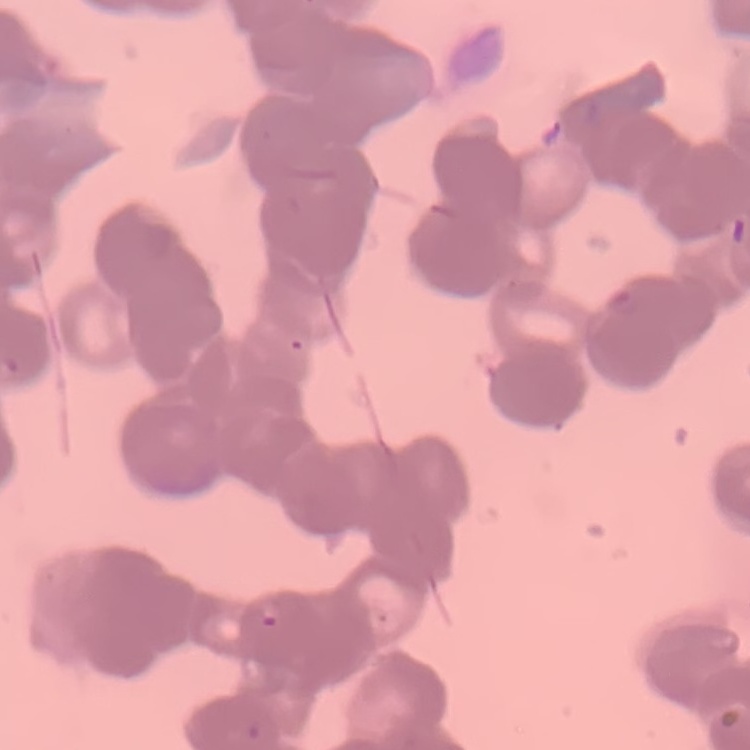
The erythrocytes exhibit rouleaux formation. Square crop of a larger photomicrograph. Stained with either Field's or Giemsa. Thin blood film.